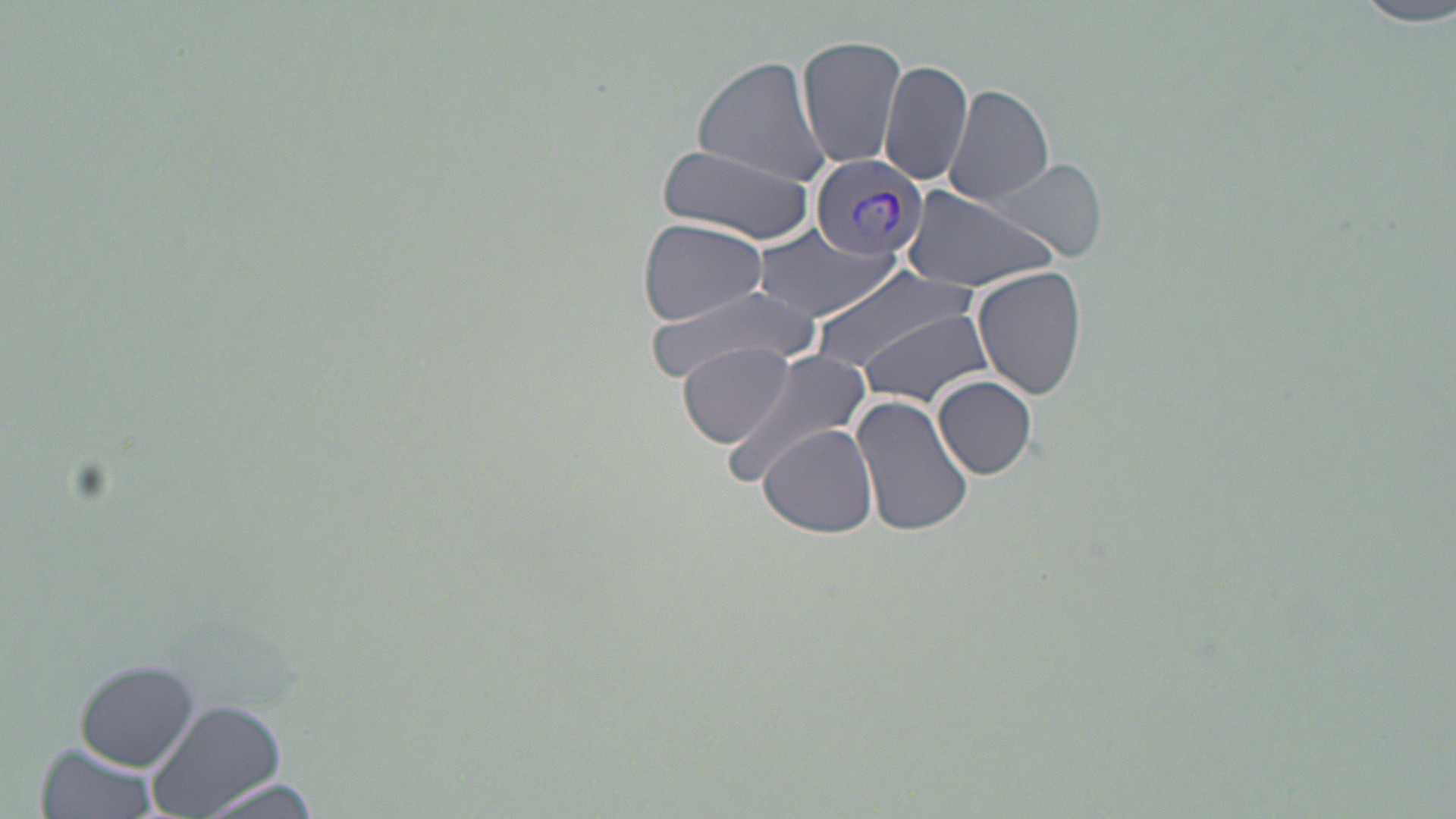

slide-level diagnosis = Plasmodium vivax
uninfected red blood cell locations = approximate bounding boxes as (x1,y1)-(x2,y2) corner pairs in pixels: (1353,2)-(1455,28), (797,34)-(907,172), (689,57)-(833,188), (879,58)-(973,188), (944,82)-(1053,206), (656,142)-(816,242), (990,159)-(1107,263), (901,184)-(1062,294), (637,216)-(768,326), (754,223)-(899,322), (809,264)-(981,377), (971,265)-(1089,400), (645,280)-(821,382), (855,309)-(996,410), (681,341)-(796,448), (722,348)-(876,483), (934,376)-(1036,480), (851,392)-(975,540), (759,424)-(880,537), (76,658)-(201,771), (147,697)-(285,818), (35,741)-(163,819), (192,778)-(324,817)
preparation = thin blood smear
magnification = 1000x
stain = May-Grünwald-Giemsa
Plasmodium vivax-infected red blood cell locations = approximate bounding boxes as (x1,y1)-(x2,y2) corner pairs in pixels: (809,152)-(928,266)
image size = 1456×819 pixels
field of view = single
modality = optical microscopy